State which parasite is depicted.
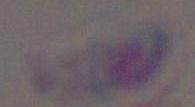
This is Toxoplasma gondii.

Photomicrograph. Captured at 1000x magnification.